Outline each Plasmodium falciparum-infected red blood cell.
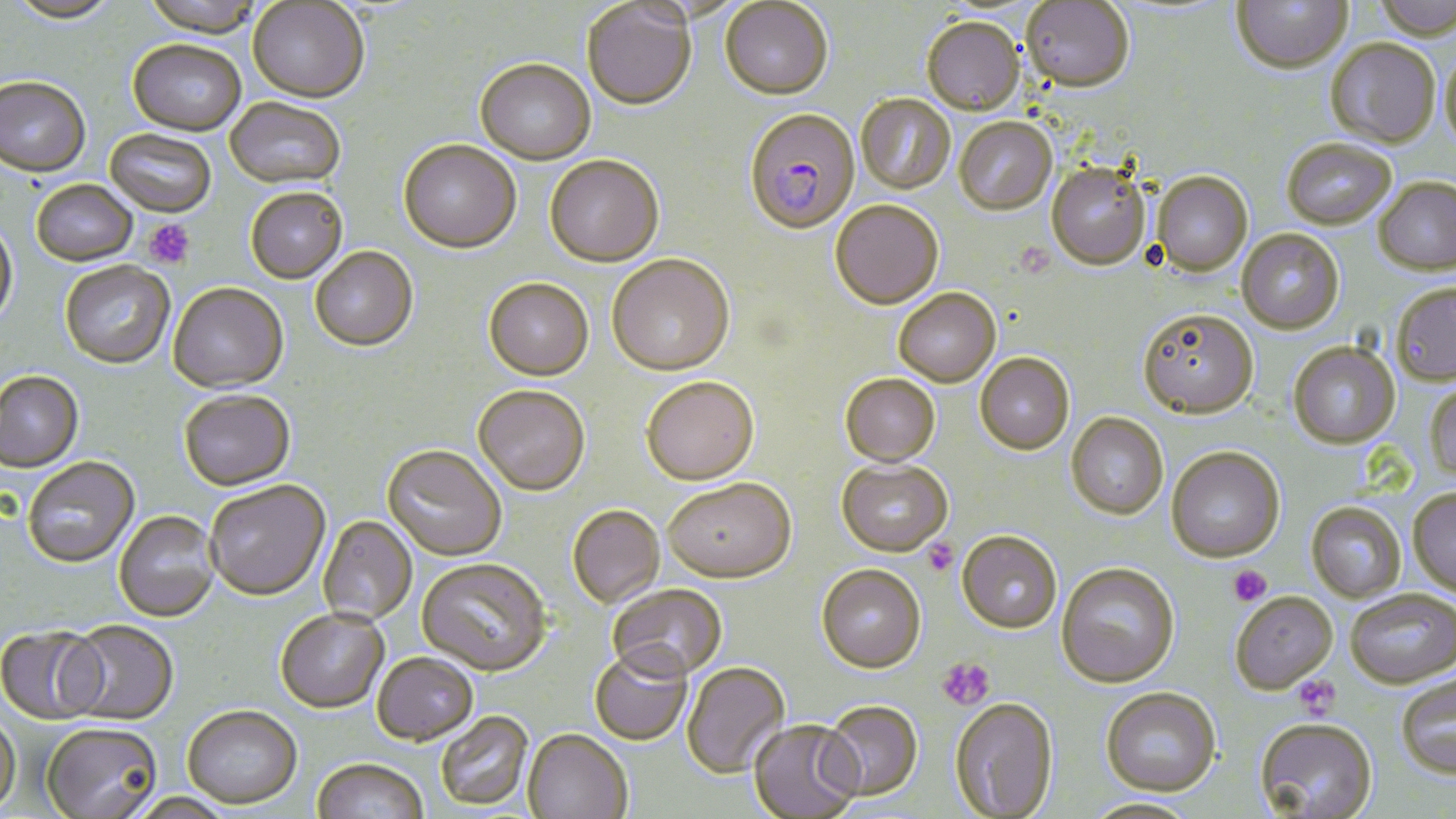

Approximate bounding boxes as (x1, y1, x2, y2) in pixels.
Plasmodium falciparum-infected red blood cells: (744, 110, 860, 236).

slide-level diagnosis = Plasmodium falciparum
image size = 1456×819 pixels
uninfected red blood cell locations = approximate bounding boxes as (x1, y1, x2, y2) in pixels: (5, 0, 122, 26), (139, 0, 266, 39), (1231, 0, 1353, 77), (1371, 0, 1456, 43), (720, 1, 833, 100), (1021, 1, 1134, 94), (248, 2, 370, 103), (582, 3, 696, 111), (922, 17, 1024, 117), (128, 40, 246, 137), (1325, 41, 1440, 150), (1439, 51, 1456, 152), (475, 60, 596, 165), (0, 78, 91, 180), (856, 94, 956, 195), (225, 98, 347, 191), (954, 119, 1057, 217), (105, 128, 216, 219), (399, 141, 521, 255), (1282, 141, 1396, 232), (545, 156, 664, 267), (1046, 165, 1151, 272), (1152, 172, 1253, 278), (1373, 178, 1456, 279), (31, 181, 138, 268), (245, 190, 347, 284), (830, 201, 943, 310), (0, 219, 18, 331), (1236, 229, 1344, 335), (310, 248, 419, 354), (607, 256, 734, 377), (60, 262, 175, 371), (483, 279, 594, 381), (1390, 283, 1456, 388), (168, 285, 289, 395), (894, 289, 1001, 388), (1137, 310, 1259, 420), (1287, 342, 1401, 451), (975, 354, 1074, 455), (0, 372, 85, 475), (840, 374, 940, 467), (641, 377, 759, 485), (1425, 381, 1456, 483), (473, 387, 590, 497), (179, 393, 295, 492), (1066, 412, 1168, 520), (381, 446, 506, 562), (1166, 447, 1285, 563), (23, 458, 140, 569), (836, 459, 953, 557), (663, 478, 795, 583), (204, 482, 330, 603), (1408, 489, 1456, 600), (1306, 502, 1406, 603), (567, 505, 665, 607), (114, 511, 220, 623), (318, 517, 417, 625), (957, 530, 1062, 634), (417, 559, 551, 677), (1056, 563, 1180, 689), (816, 565, 926, 673), (608, 584, 727, 682), (1346, 590, 1456, 690), (1230, 592, 1338, 695), (276, 610, 389, 715), (62, 622, 179, 726), (0, 627, 106, 726), (590, 648, 692, 747), (372, 654, 479, 748), (680, 662, 790, 779), (1396, 674, 1456, 780), (1100, 687, 1222, 797), (949, 698, 1059, 818), (818, 702, 923, 802), (183, 709, 302, 811), (0, 713, 21, 817), (436, 713, 534, 812), (748, 720, 862, 818), (1254, 720, 1378, 818), (40, 725, 163, 818), (522, 731, 632, 819), (311, 760, 429, 819), (126, 794, 237, 819), (1082, 798, 1200, 818)
stain = May-Grünwald-Giemsa
magnification = 1000x
preparation = thin blood smear
modality = light microscopy
platelet locations = approximate bounding boxes as (x1, y1, x2, y2) in pixels: (144, 218, 195, 269), (923, 538, 958, 576), (1229, 565, 1271, 606), (936, 657, 995, 711), (1292, 673, 1340, 718)
field of view = one of a larger specimen